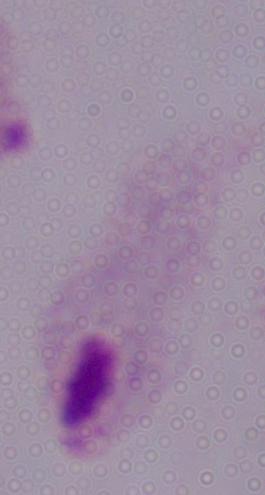

{
  "modality": "micrograph",
  "magnification": "1000x",
  "identification": "trichomonad"
}